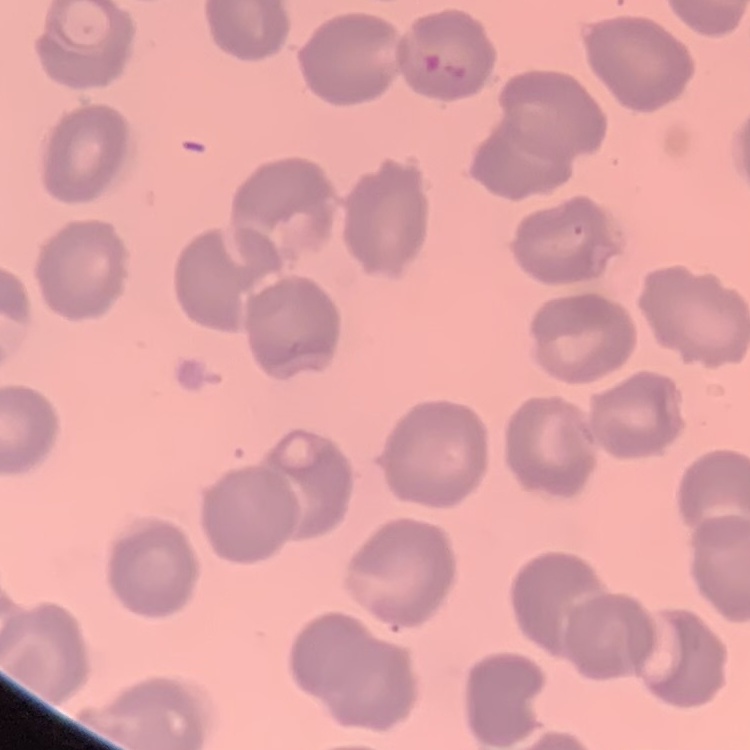

The erythrocytes exhibit no rouleaux formation. Stained with either Field's or Giemsa. Square crop of a larger photomicrograph. Thin peripheral smear.